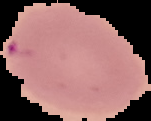
{
  "result": "Plasmodium parasites identified",
  "image_size": "151×121 pixels",
  "preparation": "thin blood film",
  "image_type": "segmented cell region on a black background"
}